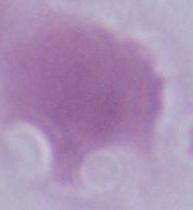
{
  "magnification": "1000x",
  "modality": "photomicrograph",
  "identification": "erythrocyte"
}